Assess this cell for malaria.
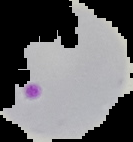
It is parasitized.

image_size: 133×142 pixels
preparation: thin blood smear
image_type: segmented cell region with the area outside set to black